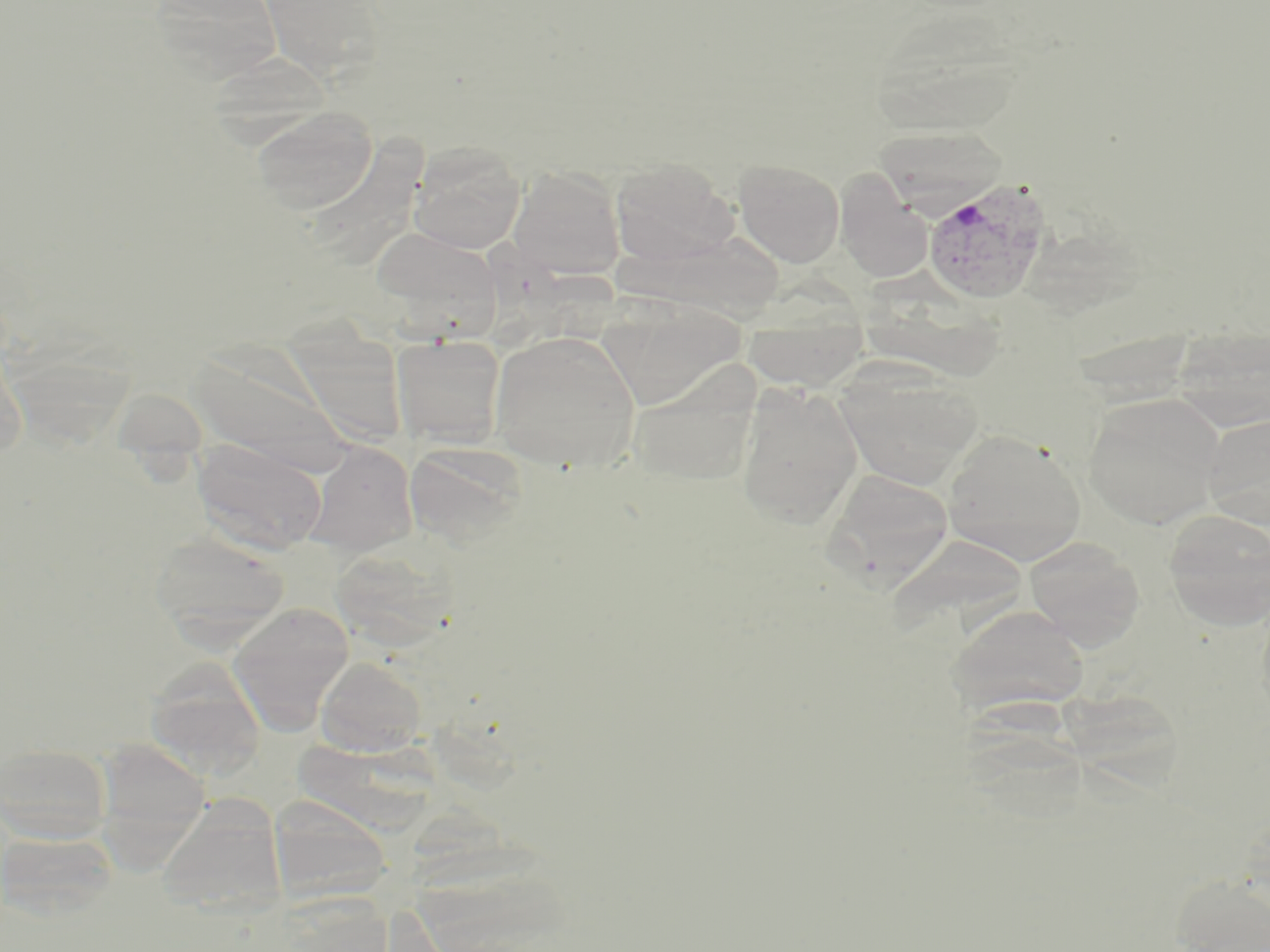
slide-level diagnosis = Plasmodium vivax
modality = light microscopy
magnification = 1000x
field of view = one of a larger specimen
Plasmodium vivax-infected red blood cell locations = approximate bounding boxes as [x1, y1, x2, y2] in pixels: [922, 177, 1053, 305]
preparation = thin blood smear
image size = 1270×952 pixels
uninfected red blood cell locations = approximate bounding boxes as [x1, y1, x2, y2] in pixels: [147, 0, 284, 84], [257, 0, 388, 82], [865, 7, 1030, 141], [251, 105, 378, 215], [409, 141, 527, 253], [611, 157, 738, 267], [733, 158, 845, 268], [508, 166, 625, 280], [835, 170, 933, 283], [367, 226, 503, 328], [596, 296, 748, 411], [743, 312, 869, 391], [489, 329, 640, 471], [391, 334, 506, 448], [185, 340, 354, 475], [628, 364, 761, 488], [835, 365, 985, 492], [735, 381, 865, 530], [1082, 392, 1227, 529], [1202, 412, 1270, 528], [939, 429, 1088, 565], [192, 437, 328, 556], [303, 441, 418, 558], [404, 442, 529, 547], [824, 468, 954, 588], [1162, 508, 1270, 629], [149, 531, 289, 643], [885, 533, 1034, 643], [1022, 535, 1146, 649], [327, 543, 459, 650], [228, 603, 355, 733], [948, 603, 1089, 716], [315, 656, 426, 757], [144, 657, 266, 779], [93, 737, 212, 856], [1, 742, 112, 845], [268, 795, 391, 906], [157, 796, 286, 920], [0, 829, 117, 921], [1170, 871, 1270, 952]
stain = May-Grünwald-Giemsa